State the blood parasite species.
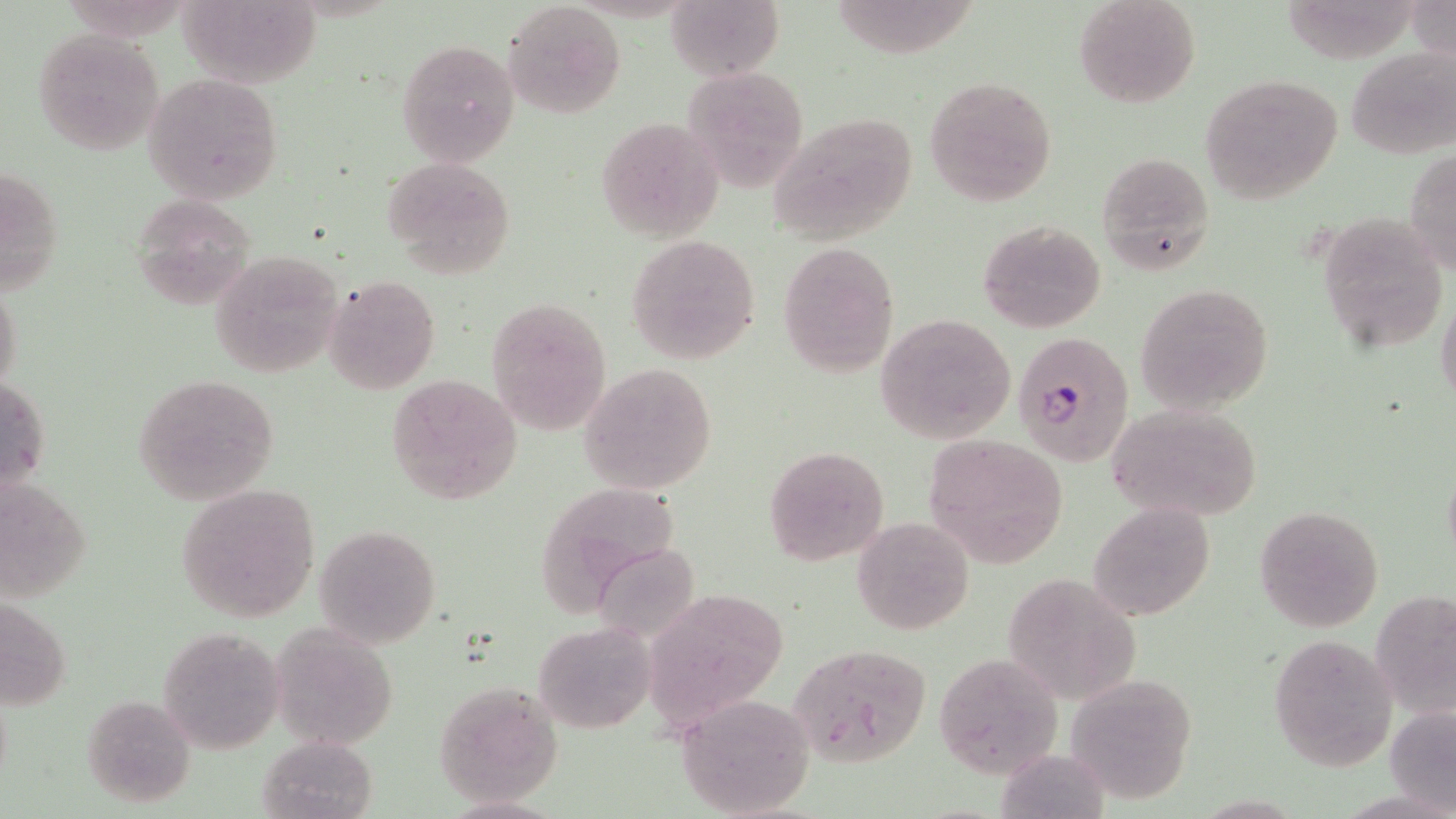

Plasmodium falciparum.

Approximate bounding boxes as [x1, y1, x2, y2] in pixels. Uninfected red blood cell locations: [176, 0, 322, 90], [665, 0, 784, 79], [1074, 0, 1201, 109], [1405, 0, 1456, 62], [503, 2, 625, 118], [33, 29, 164, 156], [396, 39, 519, 166], [1346, 46, 1456, 160], [681, 67, 810, 190], [1199, 73, 1345, 205], [142, 74, 285, 205], [923, 76, 1058, 206], [768, 111, 921, 245], [596, 116, 725, 241], [1405, 147, 1456, 276], [1095, 151, 1213, 274], [383, 156, 516, 278], [1, 162, 64, 297], [129, 193, 261, 309], [1315, 208, 1449, 350], [977, 219, 1105, 333], [625, 234, 761, 366], [778, 240, 900, 378], [210, 250, 342, 378], [324, 275, 441, 393], [0, 281, 23, 397], [1136, 284, 1274, 414], [1435, 292, 1456, 412], [486, 297, 613, 434], [874, 313, 1018, 446], [578, 364, 718, 494], [1, 373, 50, 499], [132, 373, 280, 504], [386, 374, 523, 506], [1106, 404, 1265, 522], [924, 434, 1068, 565], [764, 445, 891, 565], [1442, 461, 1456, 569], [0, 475, 95, 604], [542, 483, 678, 613], [176, 484, 321, 622], [1090, 502, 1215, 621], [1254, 506, 1384, 632], [852, 517, 975, 635], [316, 525, 440, 648], [595, 551, 700, 642], [1001, 573, 1142, 705], [1371, 586, 1456, 721], [2, 593, 72, 712], [657, 593, 794, 713], [533, 621, 656, 733], [271, 622, 401, 750], [158, 626, 286, 754], [1268, 633, 1396, 771], [786, 644, 932, 768], [934, 649, 1063, 779], [1070, 676, 1200, 805], [433, 683, 562, 806], [79, 694, 195, 808], [675, 694, 816, 819], [1385, 702, 1456, 816], [258, 735, 375, 818]. Plasmodium falciparum-infected red blood cell locations: [1012, 332, 1134, 466]. Image is 1456×819 pixels. 1000x magnification. May-Grünwald-Giemsa-stained preparation. Thin blood film. Single field of view. Light microscopy.